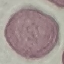

malaria status = uninfected
stain = Giemsa
image type = cell patch, automatically extracted from a larger field of view and resized to 64 × 64 pixels
preparation = thin blood smear
capture = smartphone camera at the microscope eyepiece